Report the malaria status of this cell.
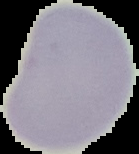
Uninfected.

image size = 139×154 pixels
image type = segmented cell region on a black background
preparation = thin blood smear